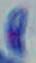

Summary:
  - Identification: Toxoplasma gondii
  - Modality: micrograph
  - Magnification: 1000x